Classify this cell by malaria status.
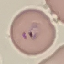
Parasitized.

Thin blood smear. Cell patch, automatically extracted from a larger field of view and resized to 64 × 64 pixels. Giemsa stain. Acquired by smartphone through the microscope eyepiece.